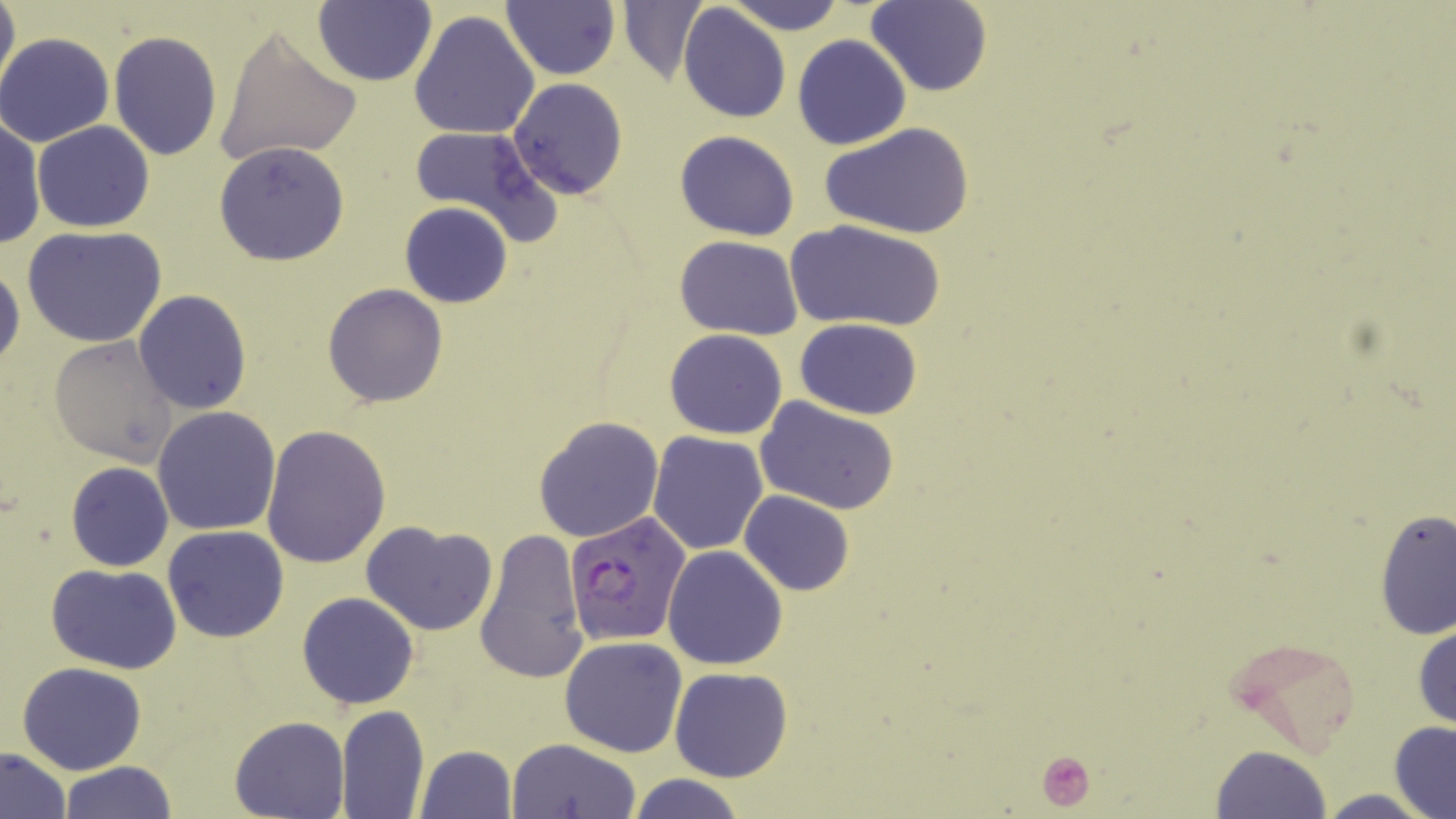
slide-level diagnosis = Plasmodium falciparum
magnification = 1000x
modality = optical microscopy
preparation = thin blood smear
uninfected red blood cell locations = approximate bounding boxes as (x1,y1)-(x2,y2) corner pairs in pixels: (1,0)-(19,100), (313,0)-(437,87), (724,0)-(847,35), (617,1)-(710,86), (866,1)-(990,96), (501,2)-(619,79), (678,4)-(790,124), (409,9)-(540,141), (213,25)-(362,170), (108,30)-(224,160), (1,32)-(117,147), (792,34)-(910,149), (508,79)-(629,198), (1,115)-(46,252), (33,121)-(155,232), (411,122)-(552,237), (821,124)-(973,240), (675,129)-(800,241), (214,141)-(349,266), (399,202)-(513,308), (786,218)-(945,333), (24,227)-(168,349), (675,236)-(804,340), (0,258)-(23,376), (322,283)-(450,407), (133,290)-(252,413), (794,318)-(921,419), (664,329)-(789,439), (50,335)-(181,467), (755,397)-(900,515), (152,406)-(282,536), (533,417)-(664,543), (260,423)-(389,567), (647,431)-(769,554), (65,462)-(175,572), (739,490)-(854,596), (1375,507)-(1455,643), (361,520)-(498,635), (162,525)-(290,642), (474,527)-(587,685), (661,544)-(787,670), (46,563)-(183,674), (297,592)-(420,709), (1412,623)-(1456,730), (1229,634)-(1363,755), (558,636)-(689,757), (16,661)-(147,775), (669,667)-(793,782), (336,704)-(430,817), (229,716)-(347,819), (1389,721)-(1456,819), (504,737)-(639,819), (415,745)-(518,818), (1210,746)-(1331,819), (1,747)-(71,818), (59,760)-(178,818), (625,773)-(750,819), (1316,789)-(1438,819)
field of view = single
Plasmodium falciparum-infected red blood cell locations = approximate bounding boxes as (x1,y1)-(x2,y2) corner pairs in pixels: (566,512)-(691,647)
stain = May-Grünwald-Giemsa
image size = 1456×819 pixels
platelet locations = approximate bounding boxes as (x1,y1)-(x2,y2) corner pairs in pixels: (1037,749)-(1097,811)